Classify this cell by malaria status.
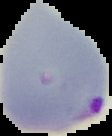
It is parasitized.

Summary:
  - Preparation: thin blood smear
  - Image size: 112×136 pixels
  - Image type: segmented cell region with the area outside set to black